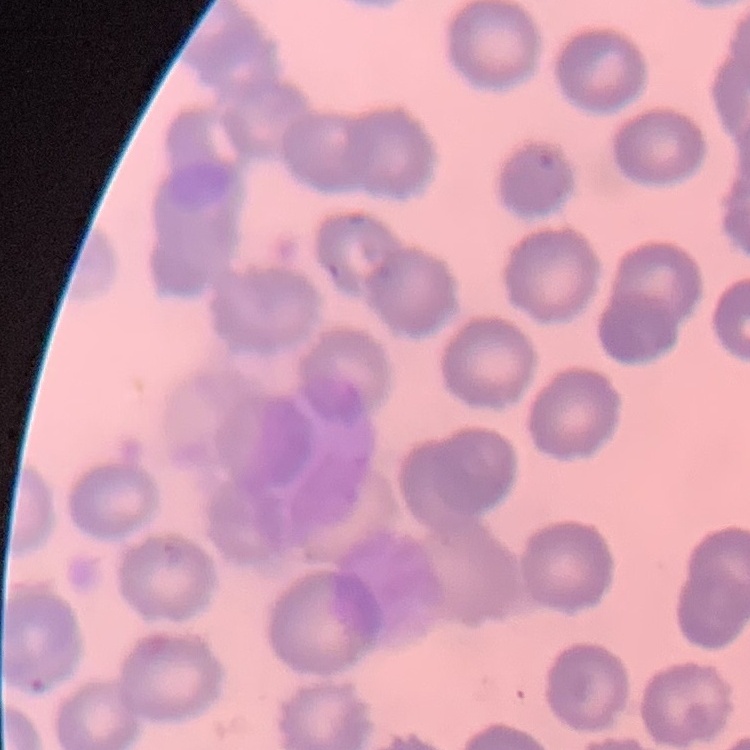

red blood cell morphology = no rouleaux formation
preparation = thin blood smear
stain = Field's or Giemsa
image type = square crop of a larger photomicrograph